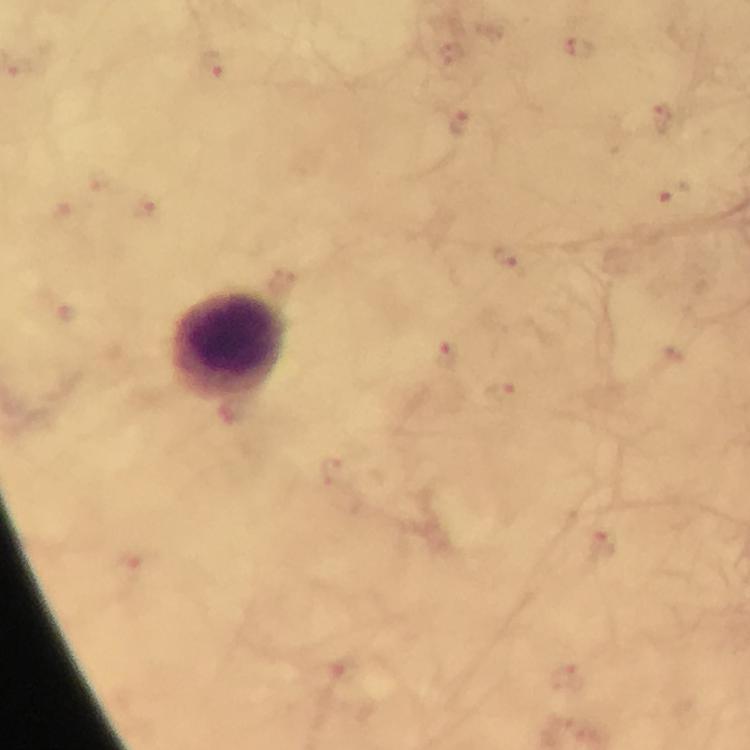

Approximate centers as [x, y] in pixels.
Summary:
  - Plasmodium parasite locations: [579, 48], [214, 64], [19, 68], [661, 118], [459, 123], [673, 193], [509, 260], [446, 356], [499, 391], [602, 544], [131, 557], [338, 672], [566, 677]
  - Leukocyte locations: [228, 346]
  - Capture: smartphone camera through the microscope
  - Context: from a diagnostic examination for malaria
  - Magnification: 100x
  - Image size: 750×750 pixels
  - Immersion oil: used
  - Preparation: thick smear
  - Cropped from: one field of view
  - Stain: Giemsa